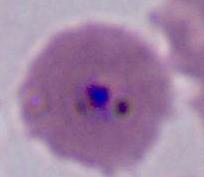

Summary:
  - Modality: micrograph
  - Identification: Plasmodium
  - Magnification: 400x or 1000x